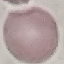

Result: negative for malaria parasites. Thin smear of blood. Cell patch, automatically extracted from a larger field of view and resized to 64 × 64 pixels. Acquired by smartphone through the microscope eyepiece. Giemsa stain.